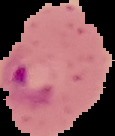

Summary:
  - Preparation: thin blood film
  - Image type: segmented cell region with the area outside set to black
  - Result: malaria parasites detected
  - Image size: 115×136 pixels